Look for Plasmodium parasites.
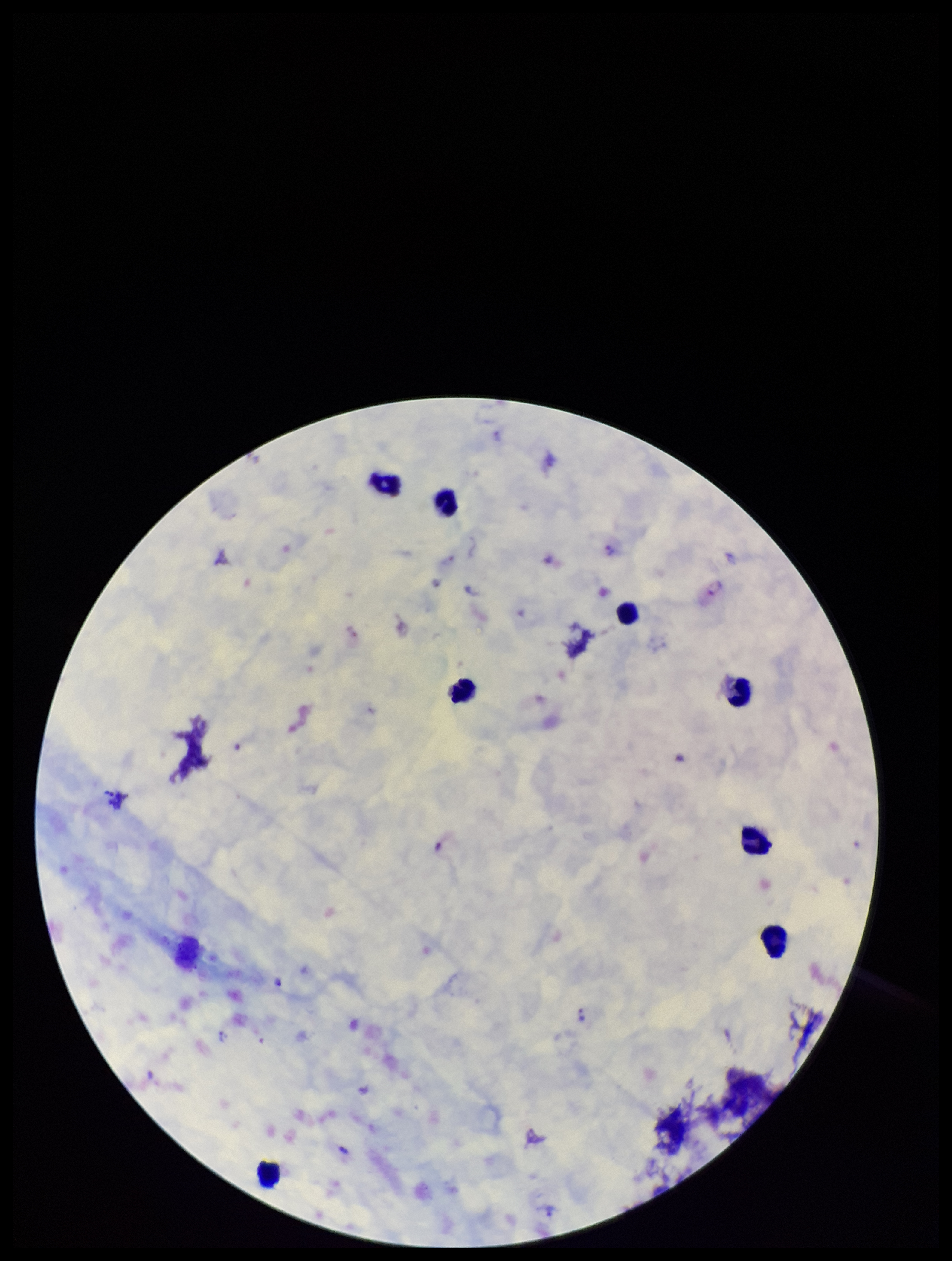
Identified.

Summary:
  - Species reported for this patient: Plasmodium vivax
  - Leukocyte count: 8
  - Preparation: thick blood smear
  - Capture: smartphone photograph through the microscope eyepiece
  - Field of view: one from this slide
  - Patient malaria status: infected
  - Stain: Giemsa
  - Image size: 952×1261 pixels
  - Parasite count: 10